Identify the parasite.
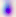

This is Toxoplasma gondii.

magnification: 400x
modality: micrograph